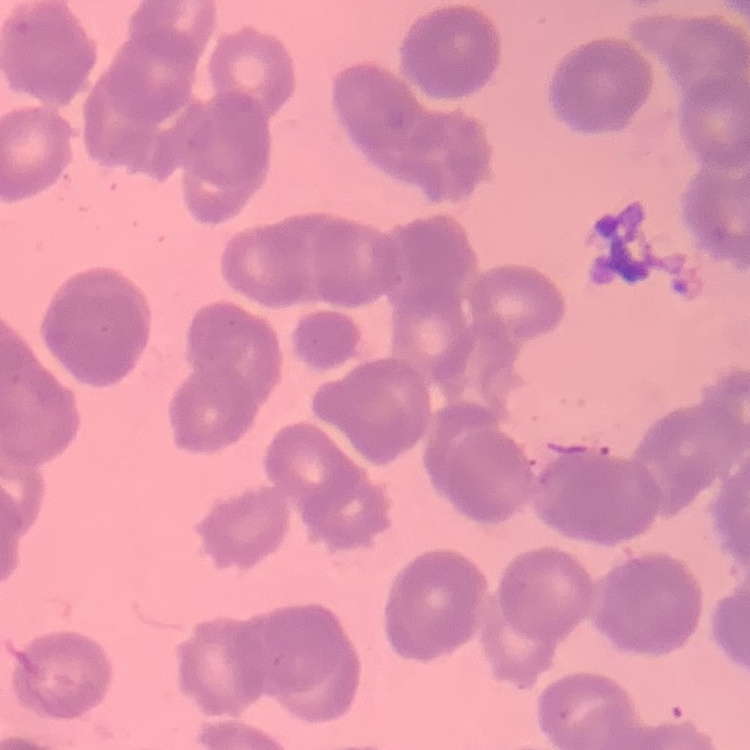

erythrocyte morphology = rouleaux formation
image type = square crop of a larger photomicrograph
stain = Field's or Giemsa
preparation = thin blood smear